Assess this cell for malaria.
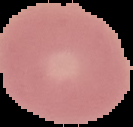
Uninfected.

Summary:
  - Image size: 133×127 pixels
  - Preparation: thin blood smear
  - Image type: segmented cell region on a black background